Assess this cell for malaria.
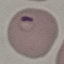
Parasitized.

stain = Giemsa
capture = smartphone through the microscope eyepiece
image type = automatically extracted cell patch, resized to 64 × 64 pixels
preparation = thin blood smear